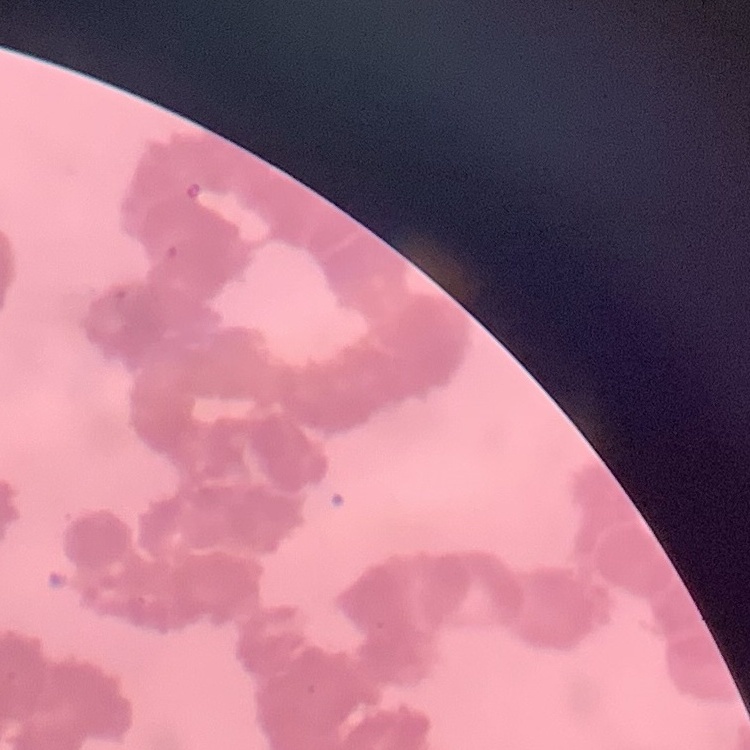
Summary:
  - Erythrocyte morphology: rouleaux formation
  - Preparation: thin peripheral smear
  - Stain: Field's or Giemsa
  - Image type: square crop of a larger photomicrograph